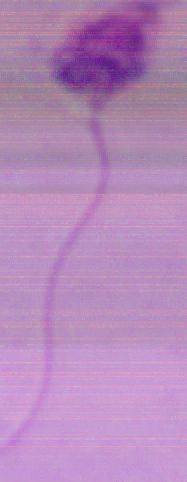
Summary:
  - Magnification: 1000x
  - Modality: photomicrograph
  - Identification: Leishmania